Assess this cell for malaria.
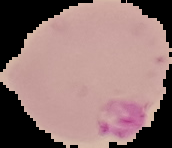
It is parasitized.

Summary:
  - Preparation: thin blood film
  - Image type: segmented cell region with the area outside set to black
  - Image size: 172×148 pixels